Outline each blood parasite and name the species.
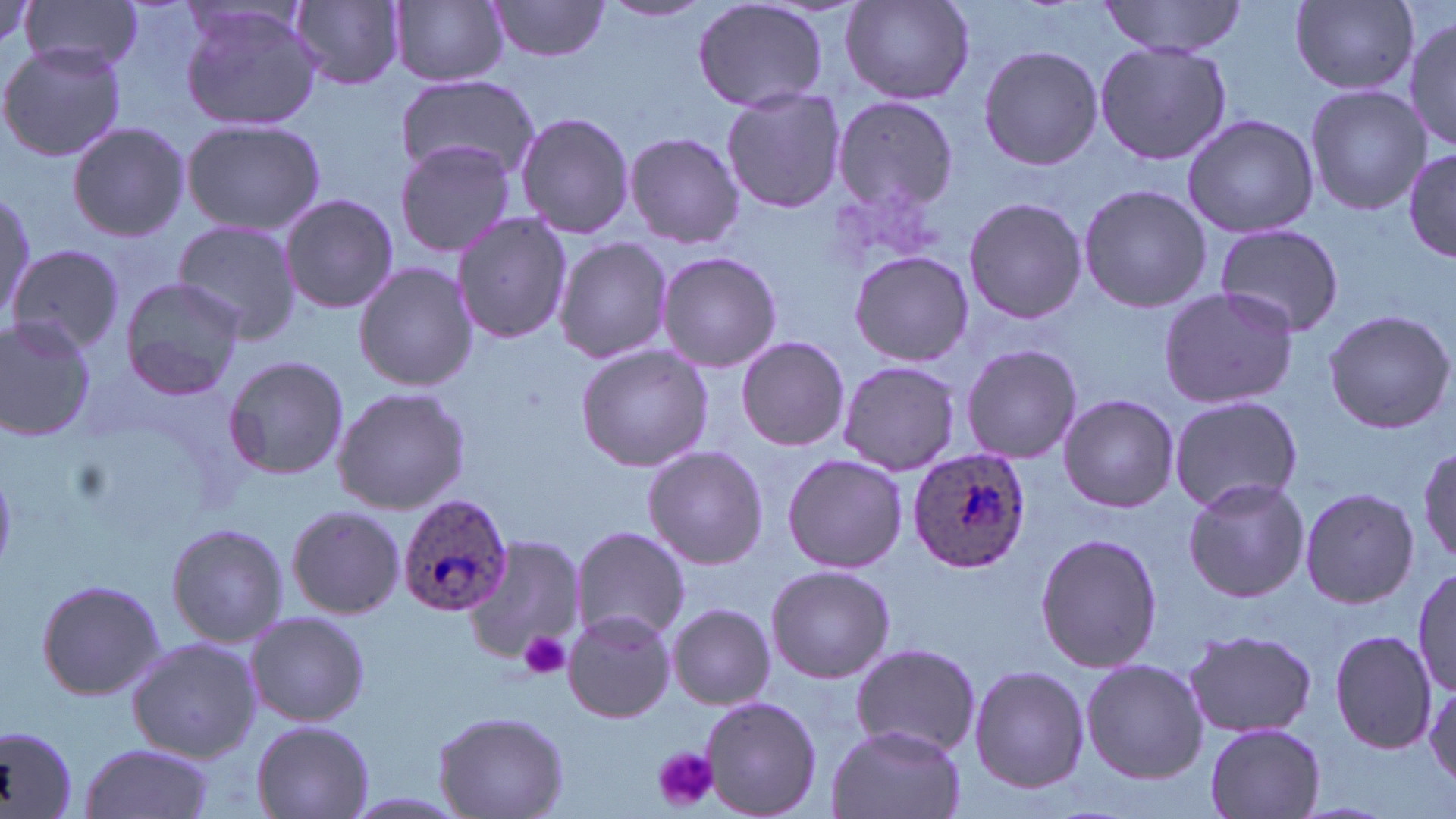

Approximate bounding boxes as [x1, y1, x2, y2] in pixels.
Plasmodium ovale-infected red blood cells: [907, 446, 1030, 574], [397, 495, 513, 617].
No Plasmodium falciparum, Plasmodium malariae, Plasmodium vivax, Babesia divergens, or Trypanosoma brucei observed.

Platelet locations: [518, 630, 572, 679], [655, 747, 717, 811]. Uninfected red blood cell locations: [22, 0, 146, 75], [692, 0, 831, 115], [838, 0, 975, 107], [294, 1, 405, 90], [391, 1, 508, 88], [599, 1, 714, 25], [1099, 1, 1246, 57], [1288, 1, 1423, 96], [487, 2, 613, 62], [176, 3, 327, 133], [1404, 15, 1456, 154], [1093, 41, 1231, 167], [0, 42, 125, 163], [977, 44, 1103, 172], [395, 75, 540, 183], [1304, 85, 1428, 214], [720, 88, 846, 214], [831, 98, 957, 213], [516, 110, 633, 240], [1181, 113, 1319, 239], [181, 119, 326, 237], [67, 121, 190, 242], [623, 131, 744, 247], [394, 138, 518, 259], [1404, 144, 1454, 265], [1077, 183, 1210, 314], [0, 192, 35, 324], [279, 193, 400, 315], [963, 197, 1088, 324], [451, 210, 573, 346], [174, 218, 301, 345], [1211, 223, 1346, 338], [553, 237, 671, 364], [7, 245, 123, 355], [655, 249, 783, 374], [848, 250, 974, 368], [353, 262, 479, 392], [118, 278, 246, 401], [1157, 284, 1298, 411], [1322, 309, 1455, 434], [0, 316, 98, 444], [736, 336, 850, 451], [574, 343, 717, 471], [960, 343, 1083, 463], [222, 354, 349, 481], [837, 359, 962, 477], [330, 387, 472, 514], [1058, 394, 1179, 513], [1167, 395, 1304, 515], [1420, 443, 1456, 568], [643, 446, 769, 570], [781, 454, 909, 573], [1181, 478, 1311, 603], [1298, 486, 1420, 608], [285, 503, 405, 620], [165, 523, 289, 648], [568, 525, 689, 644], [1034, 532, 1164, 673], [463, 537, 586, 669], [764, 564, 895, 683], [1414, 567, 1453, 701], [34, 576, 167, 702], [668, 603, 775, 709], [562, 609, 675, 723], [244, 610, 371, 727], [1329, 629, 1438, 754], [1182, 630, 1317, 740], [125, 636, 262, 762], [849, 645, 987, 757], [1080, 657, 1208, 784], [969, 665, 1090, 793], [1425, 680, 1456, 794], [699, 694, 823, 819], [432, 707, 570, 818], [250, 718, 374, 819], [1204, 722, 1327, 819], [0, 723, 79, 817], [826, 723, 966, 819], [76, 742, 216, 819]. Slide-level diagnosis: Plasmodium ovale. Optical microscopy. May-Grünwald-Giemsa stain. Captured at 1000x magnification. One field of a larger specimen. Thin blood smear. Image is 1456×819 pixels.